Locate every leukocyte (white blood cell).
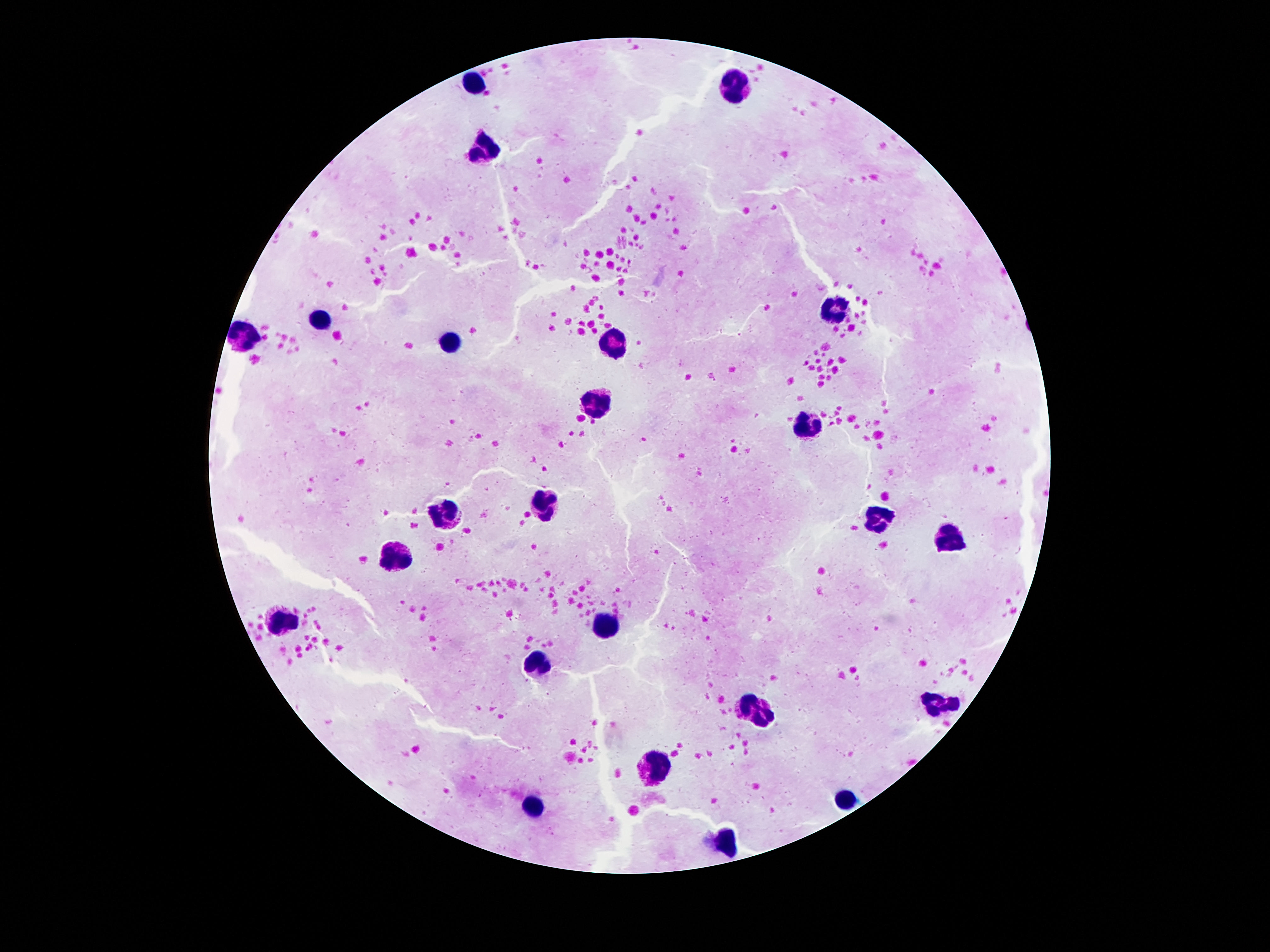
Approximate centers as (x, y) in pixels.
Leukocytes: (474, 80), (737, 82), (483, 146), (830, 307), (324, 319), (250, 334), (615, 341), (449, 345), (597, 406), (808, 425), (545, 503), (447, 512), (885, 520), (951, 536), (396, 551), (286, 622), (606, 622), (536, 663), (938, 702), (755, 711), (657, 761), (845, 799), (533, 807), (726, 840).

Image is 1270×952 pixels. 100x magnification. Thick blood smear. One field from this slide. Patient malaria status: not infected. Giemsa-stained preparation. Smartphone photograph taken through the microscope eyepiece.